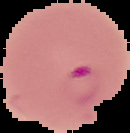
image size = 130×133 pixels
preparation = thin blood film
result = malaria parasites detected
image type = segmented cell region with the area outside set to black